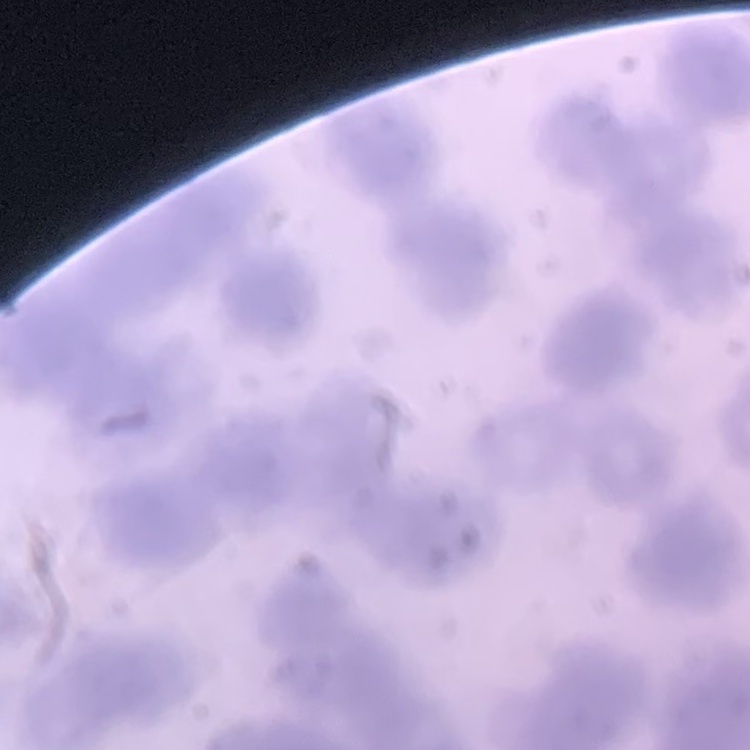 The red blood cells show rouleaux formation. Square crop of a larger photomicrograph. Stained with either Field's or Giemsa. Thin peripheral smear.